Look for Plasmodium parasites.
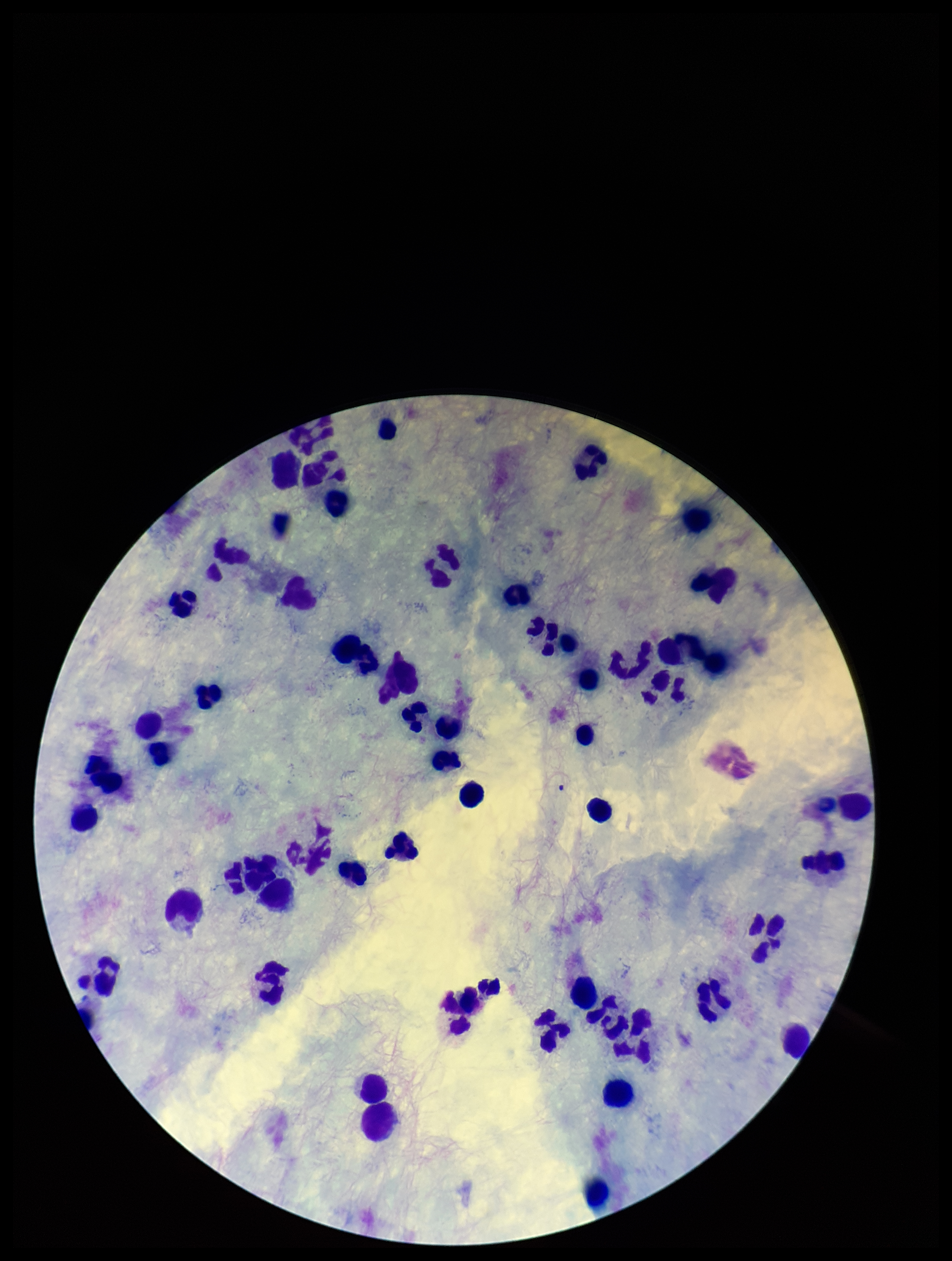

None identified.

Leukocyte count: 54. Parasite count: 0. Preparation: thick smear. Giemsa stain. Image is 952×1261 pixels. Single field of view. Smartphone photograph taken through the eyepiece of a microscope. Patient malaria status: negative.